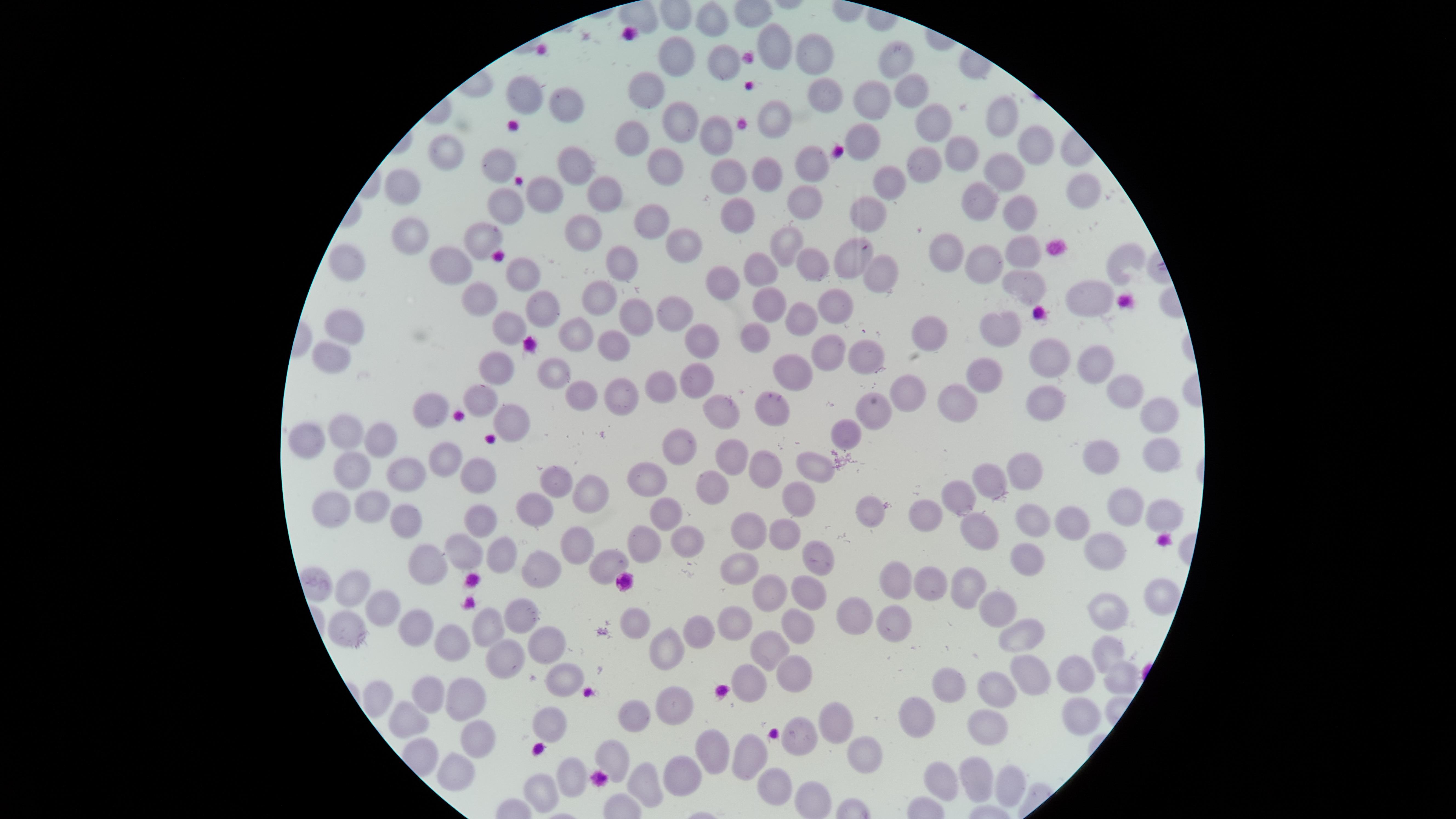

Approximate marker points as (x, y) in pixels.
Summary:
  - Uninfected red blood cells: (711, 19), (774, 42), (680, 52), (817, 57), (897, 59), (725, 62), (653, 85), (906, 91), (821, 94), (518, 97), (869, 106), (563, 108), (685, 116), (938, 119), (1007, 119), (774, 120), (715, 131), (863, 137), (627, 141), (449, 144), (1035, 144), (956, 152), (920, 156), (498, 161), (573, 162), (660, 164), (804, 170), (766, 172), (1004, 173), (731, 182), (403, 186), (608, 186), (884, 186), (1079, 190), (543, 197), (981, 199), (505, 206), (802, 206), (1018, 209), (865, 211), (739, 216), (646, 218), (584, 230), (413, 237), (482, 241), (787, 245), (681, 249), (1020, 249), (951, 251), (852, 254), (453, 262), (987, 262), (1126, 262), (624, 264), (811, 264), (344, 267), (757, 270), (519, 271), (877, 272), (725, 278), (1026, 280), (1092, 295), (474, 296), (604, 303), (766, 303), (835, 305), (539, 309), (674, 315), (802, 318), (348, 322), (637, 322), (998, 324), (508, 332), (932, 332), (572, 335), (751, 336), (693, 337), (611, 343), (824, 352), (1047, 353), (330, 354), (869, 358), (1095, 362), (980, 369), (491, 370), (550, 372), (792, 375), (693, 385), (909, 388), (662, 390), (1116, 391), (582, 393), (626, 394), (955, 397), (1044, 397), (479, 401), (435, 405), (767, 410), (881, 410), (717, 413), (1159, 413), (512, 421), (849, 425), (346, 432), (311, 436), (376, 436), (683, 440), (1163, 448), (726, 450), (1098, 455), (1099, 455), (444, 463), (810, 464), (1025, 465), (770, 467), (350, 473), (409, 476), (989, 476), (650, 478), (475, 482), (557, 482), (704, 485), (594, 491), (960, 498), (793, 499), (380, 500), (534, 502), (1122, 506), (334, 507), (664, 508), (1163, 512), (875, 513), (925, 513), (1032, 518), (481, 520), (413, 522), (1076, 524), (748, 525), (980, 531), (784, 534), (684, 541), (638, 544), (1105, 545), (460, 549), (580, 549), (499, 550), (809, 553), (1027, 557), (427, 564), (603, 564), (541, 570), (739, 570), (890, 577), (969, 577), (926, 581), (355, 586), (805, 589), (768, 591), (1154, 591), (377, 605), (1003, 607), (850, 614), (1104, 614), (522, 615), (641, 618), (887, 619), (491, 622), (735, 622), (794, 625), (413, 627), (344, 628), (698, 634), (1019, 635), (543, 638), (448, 641), (668, 645), (763, 647), (1109, 651), (502, 657), (1039, 666), (785, 672), (1081, 674), (564, 675), (1115, 675), (941, 679), (743, 685), (996, 685), (426, 692), (377, 696), (676, 697), (466, 703), (1079, 714), (547, 717), (841, 719), (914, 719), (408, 720), (640, 722), (980, 723), (798, 736), (476, 740), (616, 750), (708, 750), (741, 755), (861, 760), (453, 765), (563, 772), (682, 772), (962, 773), (771, 777), (646, 781), (1001, 783), (936, 786), (541, 793), (811, 798)
  - Preparation: thin blood film
  - Image size: 1456×819 pixels
  - Stain: Giemsa
  - Capture: smartphone photograph through the microscope eyepiece
  - Presence: no malaria parasites detected
  - Visible region: circular
  - Field of view: single